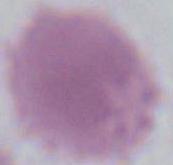

magnification = 1000x
modality = photomicrograph
identification = red blood cell